Classify this cell by malaria status.
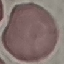
It is uninfected.

stain: Giemsa
capture: smartphone through the microscope eyepiece
image_type: cell patch, automatically extracted from a larger field of view and resized to 64 × 64 pixels
preparation: thin smear